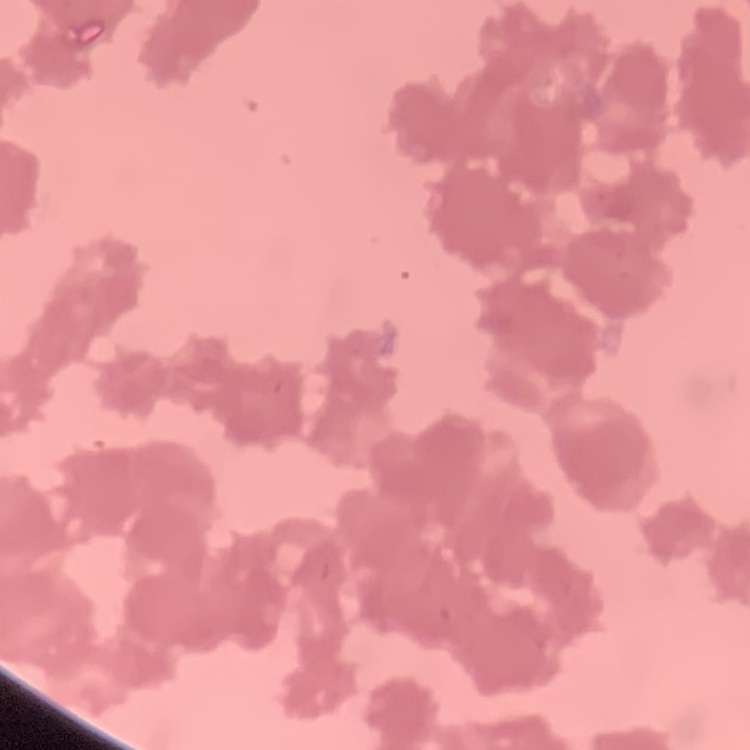

Summary:
  - Erythrocyte morphology: rouleaux formation
  - Stain: Field's or Giemsa
  - Preparation: thin blood smear
  - Image type: square crop of a larger photomicrograph